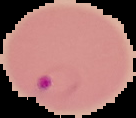
image type = segmented cell region with the area outside set to black
result = Plasmodium parasites identified
image size = 136×118 pixels
preparation = thin blood film